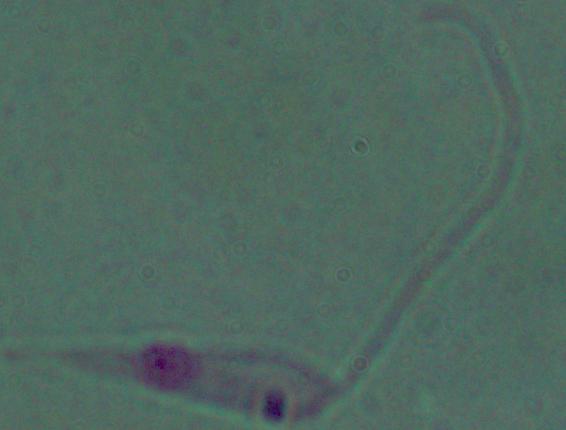 Captured at 1000x magnification. A Leishmania parasite is seen. Photomicrograph.